Report the malaria status of this cell.
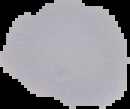

Uninfected.

Image is 130×109 pixels. Segmented cell region on a black background. From a thin blood film.